Report the malaria status of this cell.
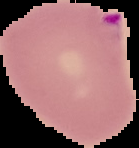

It is parasitized.

image type = cell region segmented out of the field of view; surrounding area masked to black
image size = 139×148 pixels
preparation = thin blood smear